Classify this cell by malaria status.
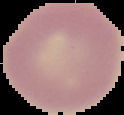
Uninfected.

Cell region segmented out of the field of view; the surrounding area is masked to black. Image is 124×115 pixels. From a thin blood smear.